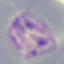

Malaria status: parasitized. Automatically extracted cell patch, resized to 64 × 64 pixels. Acquired by smartphone through the microscope eyepiece. Thin blood film. Giemsa-stained preparation.